Locate platelets.
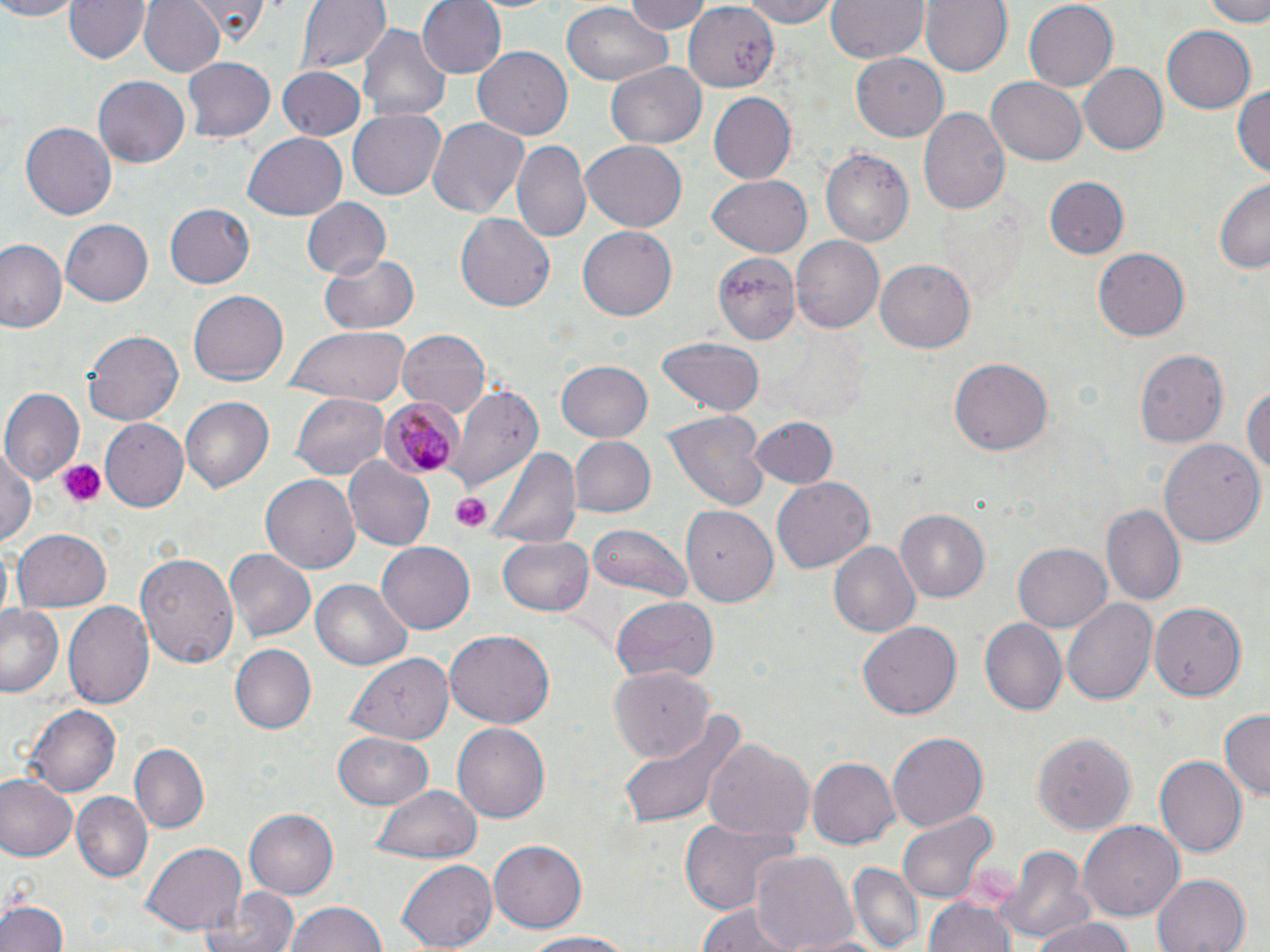

Approximate bounding boxes as named x1/y1/x2/y2 corners in pixels.
Platelets: (x1=58, y1=459, x2=108, y2=506), (x1=450, y1=493, x2=490, y2=533).

slide_level_diagnosis: Plasmodium malariae
field_of_view: one of a larger specimen
uninfected_red_blood_cell_locations: 'approximate bounding boxes as named x1/y1/x2/y2 corners in pixels: (x1=0, y1=0, x2=78, y2=21), (x1=66, y1=0, x2=150, y2=65), (x1=139, y1=0, x2=226, y2=78), (x1=185, y1=0, x2=272, y2=41), (x1=294, y1=0, x2=388, y2=76), (x1=418, y1=0, x2=505, y2=78), (x1=623, y1=0, x2=712, y2=35), (x1=729, y1=0, x2=846, y2=27), (x1=827, y1=0, x2=927, y2=64), (x1=920, y1=0, x2=1009, y2=78), (x1=1024, y1=0, x2=1117, y2=91), (x1=1204, y1=0, x2=1270, y2=26), (x1=684, y1=1, x2=781, y2=92), (x1=685, y1=4, x2=780, y2=91), (x1=561, y1=5, x2=671, y2=85), (x1=358, y1=24, x2=451, y2=125), (x1=1161, y1=26, x2=1257, y2=115), (x1=474, y1=47, x2=573, y2=141), (x1=851, y1=54, x2=948, y2=141), (x1=183, y1=56, x2=276, y2=142), (x1=606, y1=63, x2=706, y2=151), (x1=1076, y1=64, x2=1166, y2=155), (x1=276, y1=67, x2=367, y2=141), (x1=92, y1=75, x2=189, y2=168), (x1=989, y1=76, x2=1087, y2=164), (x1=1232, y1=85, x2=1270, y2=176), (x1=708, y1=92, x2=797, y2=185), (x1=348, y1=107, x2=446, y2=200), (x1=919, y1=107, x2=1010, y2=217), (x1=425, y1=118, x2=530, y2=221), (x1=21, y1=122, x2=117, y2=220), (x1=243, y1=133, x2=347, y2=219), (x1=513, y1=140, x2=590, y2=243), (x1=578, y1=140, x2=688, y2=232), (x1=820, y1=147, x2=914, y2=251), (x1=706, y1=175, x2=813, y2=257), (x1=1042, y1=177, x2=1130, y2=260), (x1=1215, y1=178, x2=1269, y2=275), (x1=302, y1=198, x2=389, y2=278), (x1=164, y1=203, x2=255, y2=288), (x1=455, y1=212, x2=557, y2=312), (x1=59, y1=219, x2=152, y2=307), (x1=578, y1=225, x2=677, y2=321), (x1=790, y1=235, x2=883, y2=334), (x1=0, y1=238, x2=67, y2=336), (x1=1094, y1=247, x2=1192, y2=340), (x1=714, y1=250, x2=801, y2=343), (x1=319, y1=252, x2=418, y2=335), (x1=875, y1=259, x2=975, y2=353), (x1=189, y1=289, x2=289, y2=385), (x1=285, y1=326, x2=414, y2=401), (x1=394, y1=328, x2=492, y2=417), (x1=84, y1=330, x2=183, y2=428), (x1=659, y1=337, x2=763, y2=415), (x1=1134, y1=348, x2=1229, y2=447), (x1=949, y1=358, x2=1053, y2=457), (x1=555, y1=361, x2=653, y2=442), (x1=1244, y1=382, x2=1270, y2=483), (x1=446, y1=383, x2=543, y2=494), (x1=1, y1=388, x2=83, y2=487), (x1=292, y1=391, x2=389, y2=481), (x1=180, y1=396, x2=274, y2=493), (x1=664, y1=413, x2=766, y2=509), (x1=751, y1=416, x2=839, y2=489), (x1=101, y1=419, x2=188, y2=515), (x1=567, y1=435, x2=654, y2=518), (x1=1158, y1=438, x2=1263, y2=547), (x1=486, y1=441, x2=580, y2=550), (x1=0, y1=444, x2=37, y2=549), (x1=344, y1=457, x2=435, y2=550), (x1=260, y1=471, x2=360, y2=572), (x1=771, y1=478, x2=875, y2=574), (x1=681, y1=502, x2=779, y2=604), (x1=1103, y1=502, x2=1185, y2=605), (x1=896, y1=508, x2=991, y2=600), (x1=585, y1=522, x2=693, y2=603), (x1=13, y1=529, x2=113, y2=612), (x1=500, y1=537, x2=596, y2=616), (x1=375, y1=540, x2=473, y2=633), (x1=829, y1=542, x2=920, y2=637), (x1=1013, y1=544, x2=1110, y2=631), (x1=224, y1=550, x2=314, y2=642), (x1=135, y1=552, x2=239, y2=667), (x1=311, y1=577, x2=412, y2=672), (x1=609, y1=595, x2=720, y2=683), (x1=1062, y1=598, x2=1159, y2=705), (x1=64, y1=601, x2=154, y2=712), (x1=1149, y1=602, x2=1246, y2=701), (x1=0, y1=605, x2=64, y2=697), (x1=978, y1=616, x2=1068, y2=715), (x1=859, y1=623, x2=962, y2=720), (x1=444, y1=632, x2=554, y2=730), (x1=233, y1=644, x2=316, y2=735), (x1=342, y1=651, x2=456, y2=747), (x1=608, y1=667, x2=714, y2=759), (x1=25, y1=703, x2=119, y2=797), (x1=1218, y1=709, x2=1269, y2=803), (x1=616, y1=713, x2=744, y2=831), (x1=453, y1=723, x2=549, y2=824), (x1=887, y1=731, x2=987, y2=831), (x1=331, y1=732, x2=434, y2=811), (x1=1032, y1=732, x2=1137, y2=834), (x1=701, y1=737, x2=814, y2=846), (x1=130, y1=742, x2=209, y2=831), (x1=807, y1=756, x2=901, y2=849), (x1=1154, y1=756, x2=1246, y2=858), (x1=0, y1=774, x2=78, y2=861), (x1=371, y1=785, x2=483, y2=863), (x1=73, y1=792, x2=152, y2=879), (x1=245, y1=809, x2=337, y2=899), (x1=898, y1=812, x2=995, y2=902), (x1=678, y1=819, x2=797, y2=920), (x1=1079, y1=821, x2=1184, y2=921), (x1=488, y1=839, x2=588, y2=934), (x1=142, y1=842, x2=246, y2=935), (x1=997, y1=845, x2=1093, y2=943), (x1=750, y1=850, x2=857, y2=952), (x1=395, y1=858, x2=499, y2=951), (x1=847, y1=864, x2=923, y2=948), (x1=1152, y1=874, x2=1250, y2=952), (x1=207, y1=888, x2=300, y2=952), (x1=925, y1=894, x2=1016, y2=952), (x1=0, y1=899, x2=67, y2=952), (x1=285, y1=902, x2=388, y2=952), (x1=696, y1=905, x2=800, y2=952), (x1=1031, y1=917, x2=1137, y2=952), (x1=519, y1=931, x2=641, y2=951), (x1=787, y1=931, x2=891, y2=951)'
plasmodium_malariae_infected_red_blood_cell_locations: 'approximate bounding boxes as named x1/y1/x2/y2 corners in pixels: (x1=379, y1=393, x2=460, y2=480)'
stain: May-Grünwald-Giemsa
preparation: thin blood smear
image_size: 1270×952 pixels
magnification: 1000x
modality: light microscopy